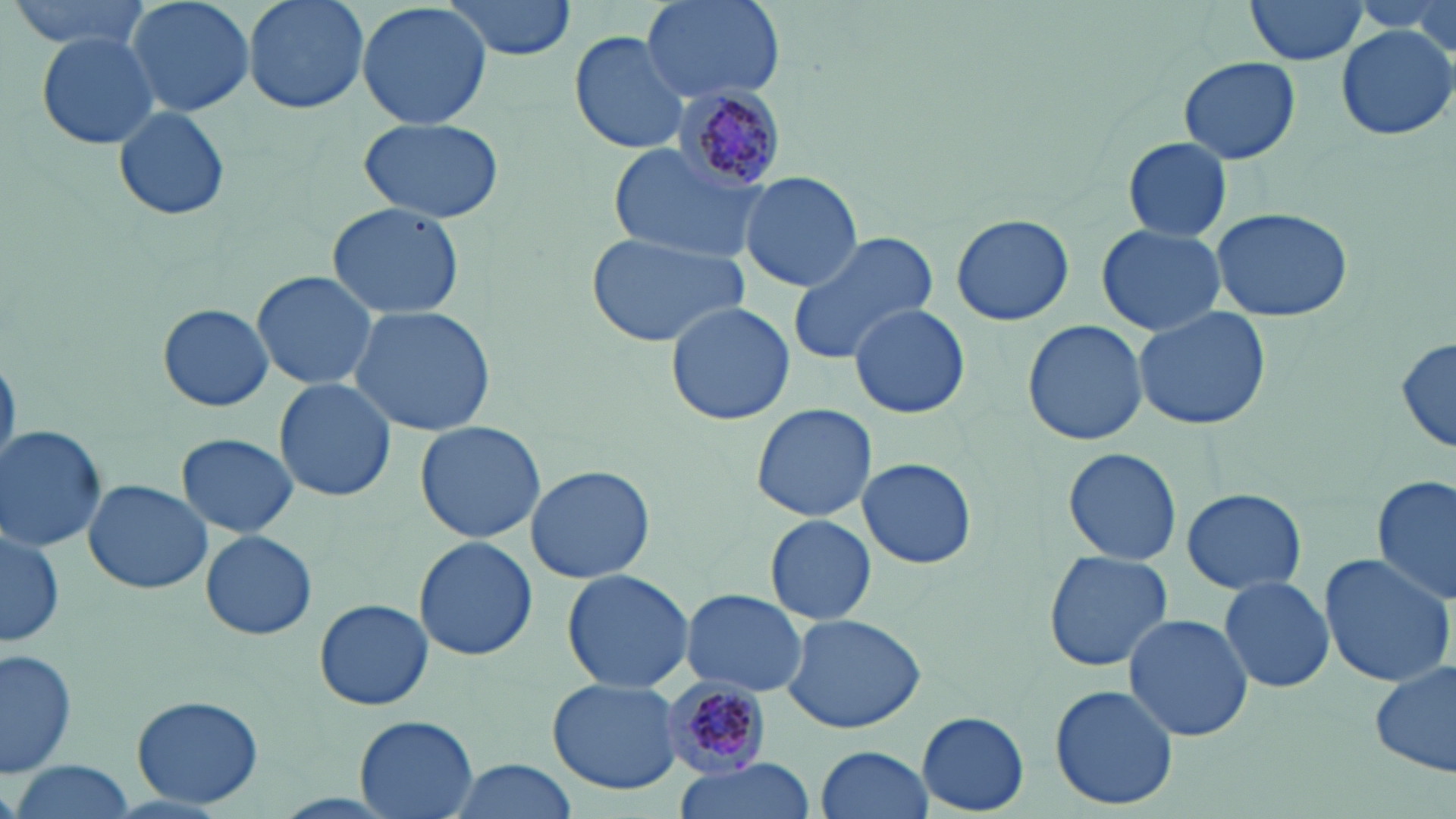 Approximate bounding boxes as (x1, y1, x2, y2) in pixels. Plasmodium malariae-infected red blood cell locations: (670, 87, 787, 195), (662, 681, 770, 777). Uninfected red blood cell locations: (7, 0, 154, 54), (123, 0, 257, 117), (241, 0, 371, 116), (356, 0, 493, 132), (443, 0, 578, 61), (642, 0, 786, 103), (1243, 0, 1372, 66), (1335, 24, 1454, 140), (568, 28, 692, 156), (35, 31, 160, 151), (1178, 56, 1300, 165), (110, 102, 233, 224), (355, 117, 505, 223), (1122, 137, 1234, 241), (610, 142, 760, 261), (739, 172, 863, 292), (324, 201, 466, 319), (1209, 206, 1356, 322), (951, 214, 1075, 327), (1095, 223, 1228, 336), (584, 231, 750, 349), (786, 231, 941, 365), (250, 270, 379, 391), (158, 303, 273, 413), (665, 303, 797, 426), (849, 304, 970, 419), (347, 305, 497, 435), (1132, 307, 1272, 432), (1022, 319, 1147, 447), (1395, 336, 1455, 457), (0, 350, 19, 478), (273, 378, 397, 502), (750, 402, 878, 523), (413, 421, 547, 543), (0, 425, 106, 552), (177, 434, 299, 537), (1063, 446, 1181, 567), (856, 457, 977, 569), (524, 464, 656, 586), (1373, 474, 1455, 606), (84, 479, 212, 595), (1181, 488, 1306, 595), (765, 514, 876, 626), (0, 529, 63, 644), (200, 529, 317, 640), (413, 537, 537, 661), (1042, 551, 1173, 673), (1317, 553, 1455, 688), (560, 568, 696, 693), (1217, 576, 1336, 693), (680, 587, 808, 697), (314, 598, 433, 711), (779, 613, 927, 734), (1123, 613, 1253, 742), (1, 647, 77, 779), (1373, 658, 1454, 777), (547, 678, 682, 793), (1049, 683, 1179, 811), (132, 693, 263, 809), (918, 711, 1030, 814), (352, 715, 479, 819), (812, 745, 932, 819), (440, 756, 585, 819), (8, 761, 138, 819), (666, 761, 814, 818). Slide-level diagnosis: Plasmodium malariae. Light microscopy. Captured at 1000x magnification. Thin blood smear. May-Grünwald-Giemsa stain. Image is 1456×819 pixels. Single field of view.